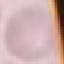

Malaria status: uninfected. Acquired by smartphone through the microscope eyepiece. Thin blood film. Cell patch, automatically extracted from a larger field of view and resized to 64 × 64 pixels. Giemsa-stained preparation.